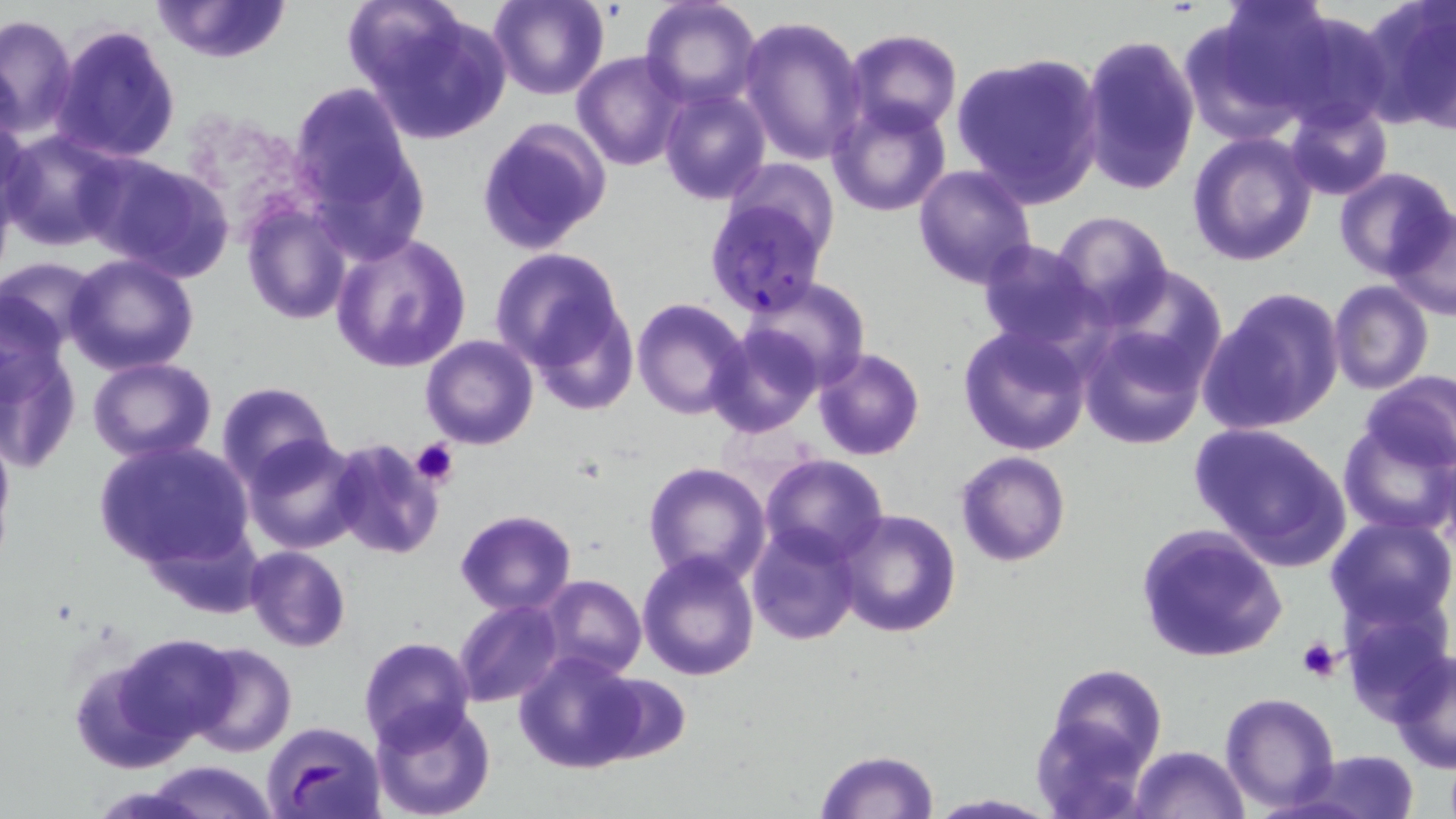

Plasmodium falciparum-infected red blood cell locations = approximate bounding boxes as (x1, y1, x2, y2) in pixels: (701, 191, 833, 320)
slide-level diagnosis = Plasmodium falciparum
image size = 1456×819 pixels
modality = optical microscopy
magnification = 1000x
preparation = thin blood film
platelet locations = approximate bounding boxes as (x1, y1, x2, y2) in pixels: (410, 437, 461, 489), (1295, 639, 1342, 682)
uninfected red blood cell locations = approximate bounding boxes as (x1, y1, x2, y2) in pixels: (149, 0, 294, 63), (489, 0, 609, 101), (639, 0, 762, 109), (1191, 0, 1338, 134), (1362, 0, 1456, 131), (350, 1, 512, 144), (1272, 10, 1394, 129), (0, 13, 78, 137), (738, 14, 868, 166), (51, 23, 182, 164), (845, 29, 962, 136), (1081, 32, 1199, 197), (952, 51, 1104, 207), (572, 52, 686, 170), (290, 82, 422, 237), (661, 88, 770, 205), (1284, 99, 1394, 201), (828, 100, 952, 216), (0, 111, 31, 231), (479, 118, 612, 256), (2, 129, 125, 251), (1188, 131, 1315, 267), (82, 153, 233, 282), (913, 164, 1038, 290), (1333, 166, 1454, 281), (241, 200, 352, 325), (1387, 208, 1456, 324), (1053, 212, 1173, 321), (330, 232, 470, 372), (975, 240, 1107, 355), (490, 247, 630, 387), (64, 253, 200, 375), (2, 256, 102, 354), (1094, 265, 1229, 389), (741, 277, 872, 392), (1328, 281, 1433, 395), (1199, 287, 1346, 436), (1, 291, 74, 409), (631, 298, 749, 420), (1079, 320, 1212, 449), (958, 325, 1093, 456), (704, 326, 821, 438), (420, 335, 538, 449), (0, 338, 82, 476), (812, 347, 924, 461), (88, 357, 218, 461), (1357, 371, 1456, 474), (216, 381, 338, 490), (0, 418, 14, 555), (1338, 418, 1454, 537), (1187, 420, 1353, 568), (243, 434, 366, 554), (326, 438, 445, 561), (93, 439, 253, 570), (955, 450, 1070, 566), (760, 454, 888, 566), (642, 461, 771, 588), (455, 508, 578, 616), (834, 508, 962, 638), (1325, 516, 1456, 634), (747, 522, 860, 645), (1134, 524, 1287, 665), (244, 546, 351, 652), (637, 552, 759, 681), (539, 575, 646, 679), (1337, 598, 1449, 723), (454, 600, 563, 708), (113, 633, 240, 745), (357, 637, 477, 752), (187, 642, 295, 757), (1387, 648, 1456, 775), (69, 649, 196, 772), (514, 652, 642, 774), (1045, 662, 1165, 786), (1220, 692, 1340, 810), (369, 700, 496, 819), (262, 721, 386, 819), (1131, 743, 1249, 819), (814, 749, 940, 819), (1300, 750, 1420, 819), (139, 760, 280, 819), (924, 792, 1059, 818)
stain = May-Grünwald-Giemsa
field of view = one of a larger specimen